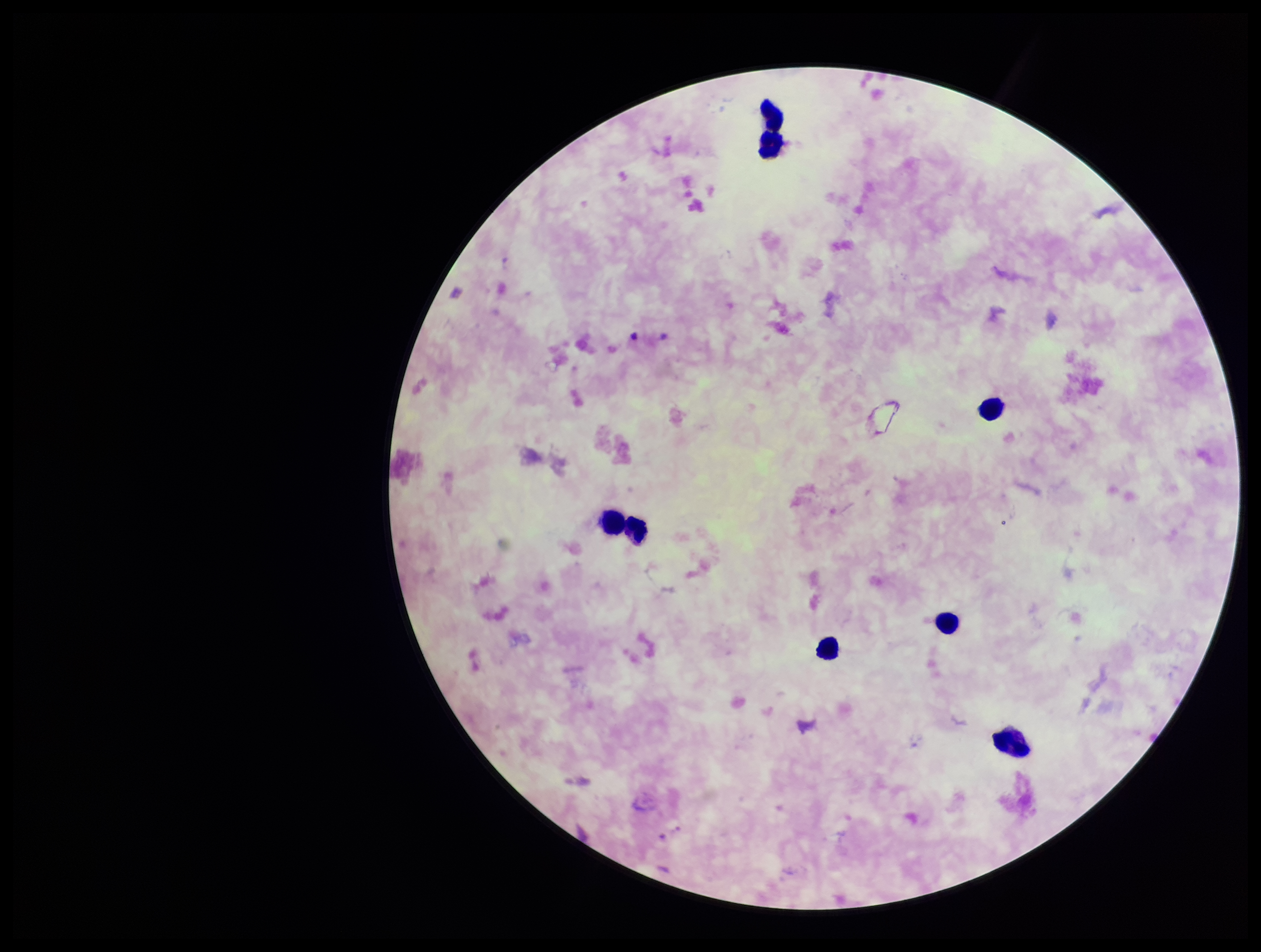

parasite count = 0
field of view = single
patient malaria status = positive
preparation = thick blood smear
leukocyte count = 8
species reported for this patient = Plasmodium falciparum
capture = smartphone photograph through the microscope eyepiece
stain = Giemsa
image size = 1261×952 pixels
Plasmodium parasites = none identified